Locate every blood parasite and identify its species.
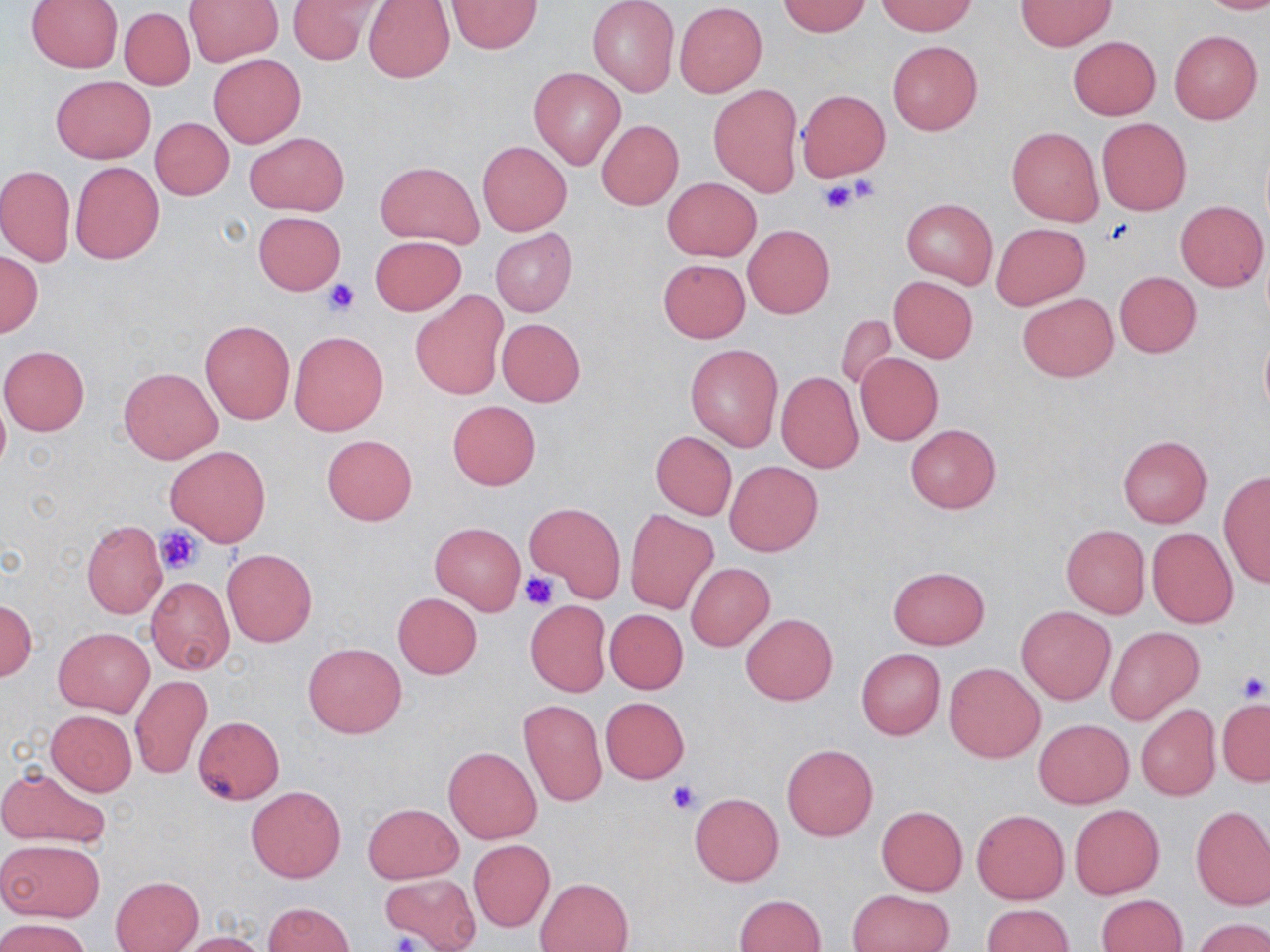

No blood parasites seen.

slide-level diagnosis = no evidence of blood parasites
modality = light microscopy
image size = 1270×952 pixels
uninfected red blood cell locations = approximate bounding boxes as (x1, y1, x2, y2) in pixels: (185, 0, 282, 65), (288, 0, 380, 66), (363, 0, 455, 84), (447, 0, 543, 54), (587, 0, 679, 97), (1198, 0, 1270, 15), (27, 1, 123, 72), (778, 1, 870, 36), (881, 1, 973, 36), (1016, 1, 1115, 50), (674, 2, 768, 98), (119, 8, 194, 90), (1168, 30, 1262, 125), (1068, 36, 1160, 119), (888, 41, 982, 136), (208, 53, 305, 148), (529, 67, 625, 168), (51, 75, 155, 163), (709, 84, 802, 196), (798, 89, 890, 182), (151, 117, 233, 200), (1097, 118, 1192, 216), (597, 120, 682, 210), (1006, 125, 1103, 225), (245, 132, 349, 216), (477, 141, 571, 235), (70, 161, 164, 264), (377, 161, 484, 248), (0, 164, 74, 267), (663, 177, 760, 261), (901, 198, 997, 290), (1174, 200, 1268, 292), (254, 212, 345, 294), (991, 222, 1089, 309), (743, 225, 834, 319), (491, 228, 576, 317), (370, 236, 466, 316), (0, 249, 43, 338), (657, 259, 750, 343), (1113, 271, 1201, 357), (888, 276, 978, 362), (411, 292, 506, 400), (1018, 293, 1117, 382), (836, 313, 897, 392), (496, 318, 586, 406), (200, 319, 295, 424), (1259, 329, 1270, 421), (290, 331, 387, 436), (686, 344, 783, 451), (0, 346, 89, 436), (855, 353, 943, 445), (119, 366, 221, 463), (776, 371, 864, 473), (447, 400, 540, 489), (905, 425, 1001, 514), (651, 431, 737, 520), (322, 434, 417, 525), (1117, 435, 1212, 527), (166, 445, 271, 546), (725, 460, 822, 555), (1218, 472, 1270, 588), (525, 502, 624, 599), (625, 510, 718, 614), (82, 520, 167, 619), (431, 523, 525, 614), (1060, 524, 1150, 618), (1147, 527, 1239, 627), (222, 548, 317, 646), (686, 562, 775, 652), (888, 566, 989, 648), (146, 576, 234, 676), (393, 592, 482, 680), (0, 599, 37, 681), (525, 601, 611, 696), (1017, 605, 1115, 705), (605, 609, 688, 694), (741, 614, 837, 706), (54, 627, 153, 716), (1106, 627, 1203, 724), (303, 642, 406, 738), (856, 649, 945, 739), (944, 663, 1045, 763), (129, 675, 212, 779), (600, 697, 690, 784), (520, 698, 608, 806), (1217, 699, 1269, 785), (1135, 704, 1220, 801), (47, 710, 136, 795), (193, 716, 285, 804), (1034, 719, 1133, 809), (782, 744, 878, 840), (444, 746, 541, 842), (0, 765, 111, 848), (246, 785, 345, 883), (689, 794, 784, 886), (364, 803, 461, 883), (1070, 804, 1164, 898), (876, 806, 968, 896), (1191, 806, 1270, 909), (972, 810, 1069, 904), (0, 838, 105, 923), (469, 840, 554, 931), (380, 873, 481, 951), (110, 876, 204, 952), (536, 877, 632, 952), (848, 889, 954, 952), (735, 894, 826, 952), (1096, 894, 1186, 952), (263, 902, 355, 952), (981, 903, 1072, 952), (0, 918, 91, 952), (1194, 918, 1270, 951), (180, 933, 268, 952)
preparation = thin blood film
field of view = single
stain = May-Grünwald-Giemsa
magnification = 1000x
platelet locations = approximate bounding boxes as (x1, y1, x2, y2) in pixels: (845, 173, 881, 203), (818, 178, 861, 215), (323, 279, 360, 316), (155, 528, 204, 573), (519, 571, 558, 609), (1234, 668, 1269, 703), (665, 778, 702, 814), (387, 930, 425, 952)